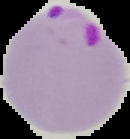

Summary:
  - Malaria status: parasitized
  - Image type: segmented cell region with the area outside set to black
  - Image size: 130×139 pixels
  - Preparation: thin blood film